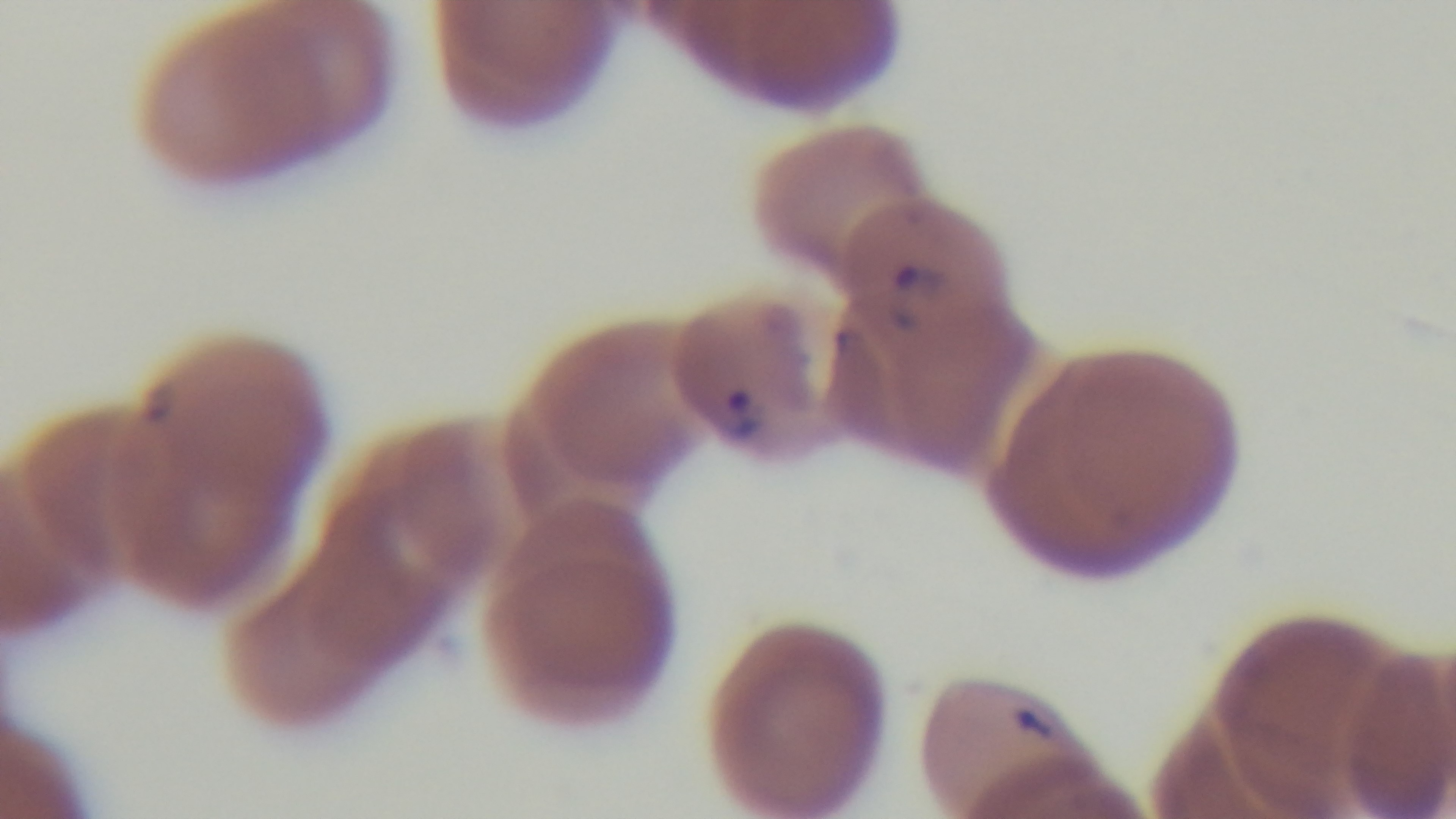
{
  "malaria_status": "infected",
  "stain": "Giemsa",
  "modality": "light microscopy",
  "field_of_view": "single",
  "preparation": "thin smear",
  "capture": "mounted 4K digital camera",
  "objective": "100x oil immersion"
}